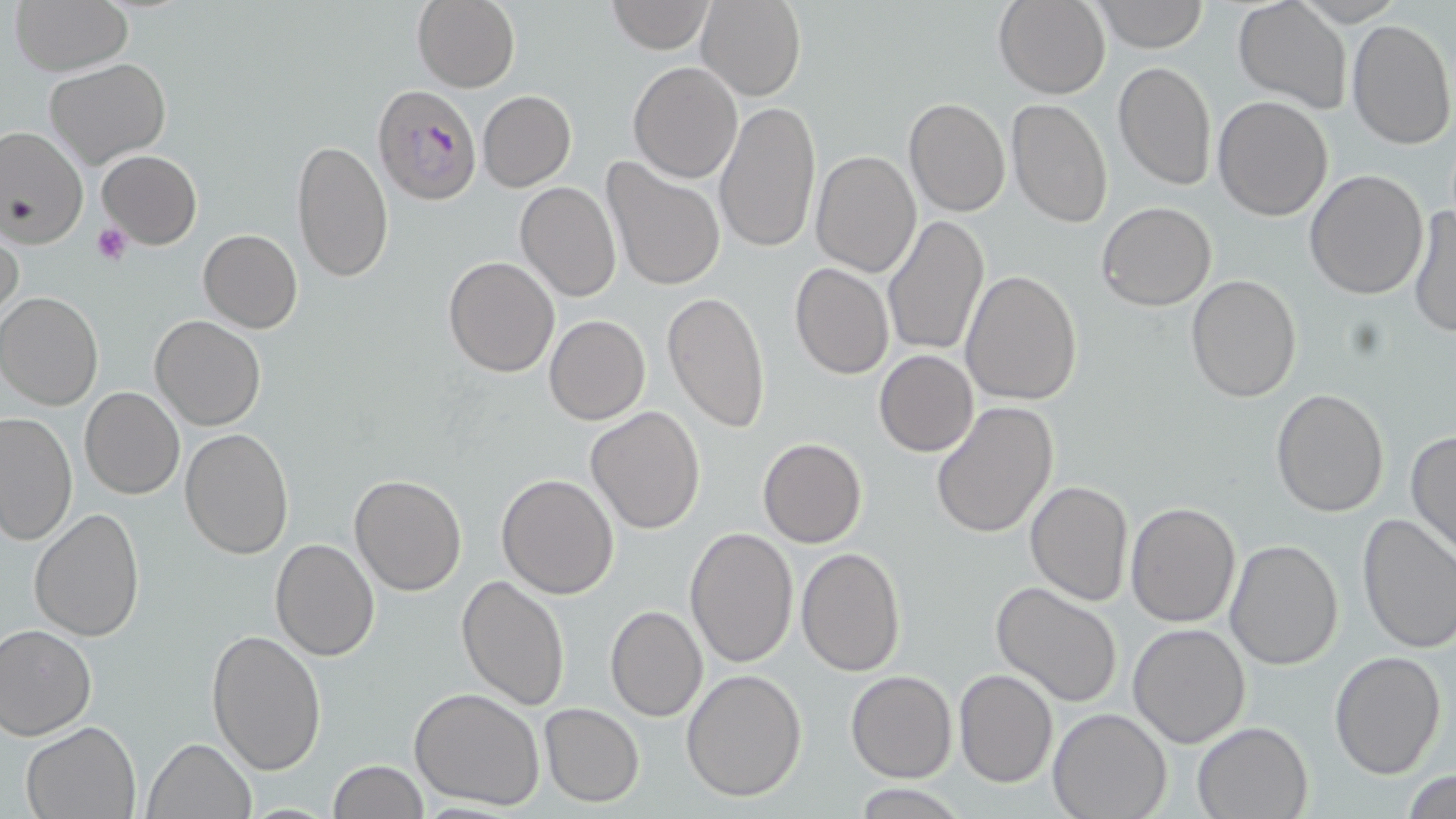
Summary:
  - Coordinate format: approximate bounding boxes as (x1,y1)-(x2,y2) corner pairs in pixels
  - Plasmodium falciparum-infected red blood cell locations: (371,84)-(481,205)
  - Uninfected red blood cell locations: (10,0)-(132,75), (412,0)-(521,93), (607,0)-(713,53), (1094,0)-(1207,51), (699,1)-(805,100), (993,1)-(1110,99), (1232,1)-(1353,113), (1295,1)-(1404,25), (1345,17)-(1455,149), (44,59)-(170,170), (1113,59)-(1216,192), (629,62)-(743,183), (478,90)-(576,191), (1212,95)-(1333,222), (1008,97)-(1112,231), (715,99)-(821,254), (903,99)-(1011,219), (0,127)-(86,251), (293,139)-(393,281), (97,150)-(202,248), (811,151)-(922,277), (601,158)-(727,293), (1304,169)-(1430,299), (515,182)-(621,301), (1097,201)-(1217,311), (1407,205)-(1455,339), (882,215)-(991,359), (0,225)-(25,331), (198,229)-(302,332), (443,255)-(559,376), (790,263)-(893,379), (960,269)-(1083,406), (1186,275)-(1301,404), (0,291)-(103,411), (662,291)-(771,434), (150,314)-(266,431), (544,315)-(650,424), (874,350)-(979,457), (80,387)-(185,499), (1270,388)-(1391,517), (930,400)-(1059,541), (586,405)-(706,535), (0,410)-(77,547), (179,427)-(295,559), (1407,429)-(1456,559), (757,437)-(867,548), (496,473)-(619,598), (350,474)-(466,594), (1025,480)-(1134,605), (1125,501)-(1241,627), (27,508)-(145,643), (1356,512)-(1456,653), (684,527)-(798,669), (269,538)-(379,660), (1223,538)-(1344,669), (795,548)-(906,677), (456,576)-(571,712), (990,582)-(1124,708), (604,605)-(707,722), (0,623)-(98,740), (1128,623)-(1251,747), (206,630)-(327,777), (1330,648)-(1447,778), (953,668)-(1059,787), (681,669)-(807,802), (846,669)-(956,783), (410,687)-(547,811), (540,703)-(644,806), (1048,709)-(1172,819), (20,720)-(144,818), (1192,721)-(1311,818), (142,737)-(255,819), (329,760)-(428,818), (1404,769)-(1455,819), (853,782)-(968,818)
  - Platelet locations: (91,222)-(131,266)
  - Slide-level diagnosis: Plasmodium falciparum
  - Image size: 1456×819 pixels
  - Preparation: thin blood smear
  - Stain: May-Grünwald-Giemsa
  - Magnification: 1000x
  - Modality: optical microscopy
  - Field of view: one of a larger specimen